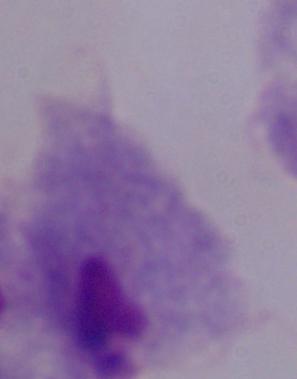

A trichomonad is seen. 1000x magnification. Micrograph.